Give the extent of all uninfected red blood cells.
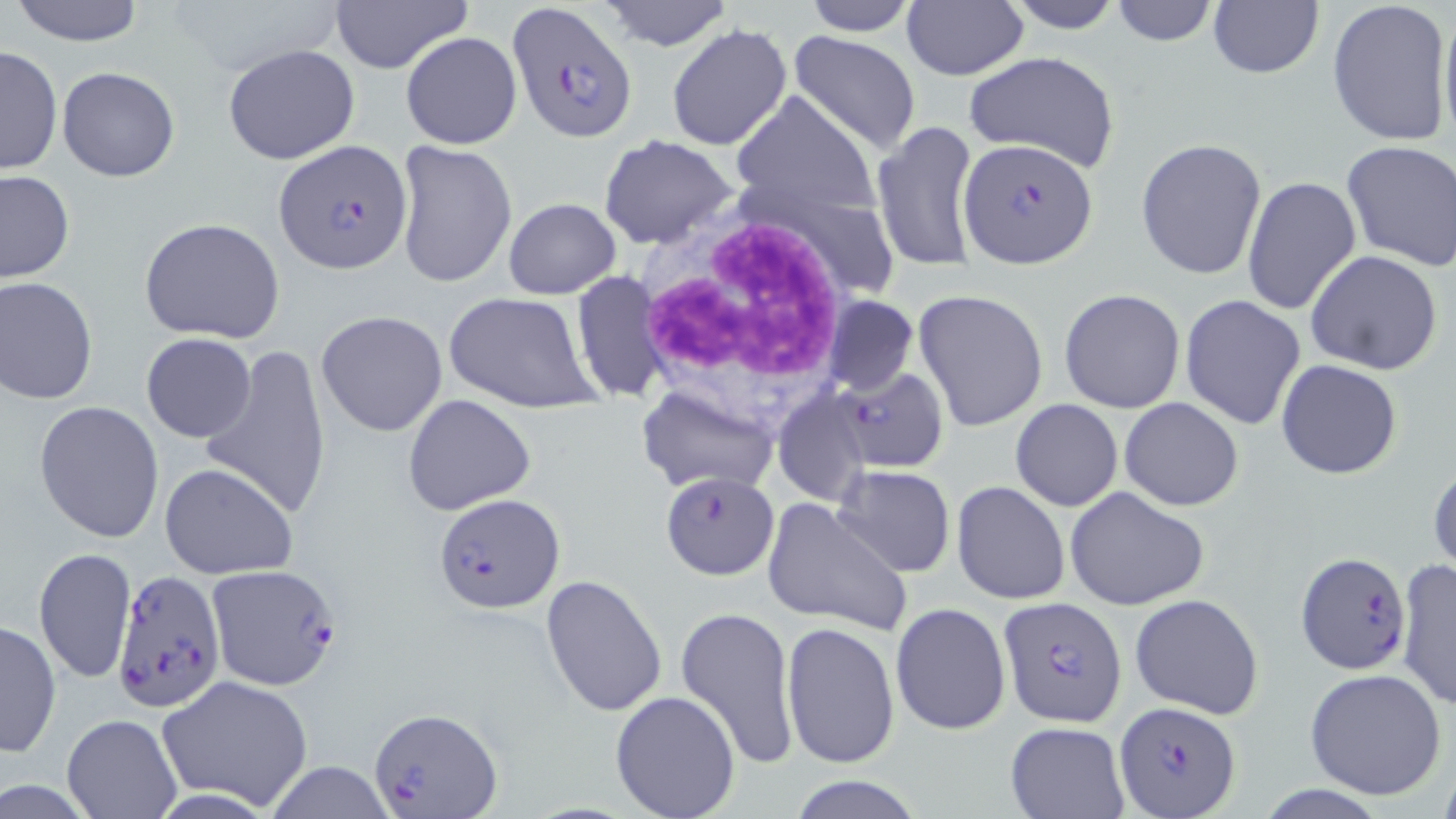

Approximate bounding boxes as named x1/y1/x2/y2 corners in pixels.
Uninfected red blood cells: (x1=7, y1=0, x2=147, y2=47), (x1=326, y1=0, x2=474, y2=73), (x1=598, y1=0, x2=735, y2=50), (x1=800, y1=0, x2=921, y2=36), (x1=1002, y1=0, x2=1128, y2=34), (x1=1109, y1=0, x2=1219, y2=47), (x1=1327, y1=0, x2=1453, y2=147), (x1=1207, y1=1, x2=1325, y2=80), (x1=1438, y1=1, x2=1456, y2=151), (x1=902, y1=2, x2=1029, y2=81), (x1=666, y1=24, x2=791, y2=152), (x1=789, y1=30, x2=922, y2=154), (x1=400, y1=32, x2=522, y2=150), (x1=1, y1=44, x2=61, y2=178), (x1=223, y1=44, x2=362, y2=166), (x1=964, y1=52, x2=1122, y2=173), (x1=56, y1=65, x2=180, y2=181), (x1=731, y1=89, x2=883, y2=222), (x1=872, y1=119, x2=981, y2=274), (x1=597, y1=134, x2=739, y2=249), (x1=1136, y1=138, x2=1268, y2=280), (x1=1341, y1=138, x2=1456, y2=271), (x1=392, y1=140, x2=517, y2=292), (x1=0, y1=170, x2=73, y2=285), (x1=1241, y1=175, x2=1363, y2=316), (x1=504, y1=198, x2=622, y2=300), (x1=138, y1=217, x2=286, y2=344), (x1=1305, y1=249, x2=1444, y2=375), (x1=572, y1=271, x2=666, y2=403), (x1=0, y1=276, x2=99, y2=404), (x1=1058, y1=288, x2=1187, y2=413), (x1=915, y1=290, x2=1048, y2=433), (x1=444, y1=291, x2=601, y2=414), (x1=1180, y1=294, x2=1307, y2=432), (x1=822, y1=296, x2=919, y2=395), (x1=316, y1=311, x2=448, y2=436), (x1=141, y1=332, x2=257, y2=442), (x1=200, y1=346, x2=334, y2=518), (x1=1277, y1=359, x2=1404, y2=480), (x1=638, y1=385, x2=778, y2=497), (x1=773, y1=388, x2=873, y2=506), (x1=402, y1=393, x2=537, y2=516), (x1=1120, y1=397, x2=1244, y2=511), (x1=1010, y1=398, x2=1123, y2=511), (x1=35, y1=400, x2=165, y2=542), (x1=1429, y1=457, x2=1456, y2=578), (x1=158, y1=462, x2=297, y2=579), (x1=832, y1=465, x2=955, y2=577), (x1=952, y1=481, x2=1070, y2=604), (x1=1064, y1=486, x2=1210, y2=611), (x1=762, y1=496, x2=913, y2=636), (x1=32, y1=547, x2=135, y2=687), (x1=1396, y1=561, x2=1456, y2=709), (x1=539, y1=574, x2=669, y2=718), (x1=1130, y1=592, x2=1265, y2=719), (x1=890, y1=602, x2=1011, y2=736), (x1=676, y1=605, x2=799, y2=770), (x1=1, y1=619, x2=62, y2=757), (x1=783, y1=621, x2=899, y2=769), (x1=1304, y1=668, x2=1446, y2=798), (x1=157, y1=674, x2=314, y2=812), (x1=610, y1=690, x2=742, y2=819), (x1=62, y1=714, x2=180, y2=818), (x1=1005, y1=721, x2=1129, y2=818), (x1=265, y1=762, x2=397, y2=819), (x1=787, y1=774, x2=928, y2=818).

White blood cell locations: (x1=633, y1=206, x2=856, y2=441). Plasmodium falciparum-infected red blood cell locations: (x1=507, y1=1, x2=638, y2=142), (x1=960, y1=138, x2=1097, y2=268), (x1=275, y1=141, x2=414, y2=274), (x1=834, y1=367, x2=950, y2=473), (x1=660, y1=471, x2=779, y2=579), (x1=432, y1=491, x2=562, y2=610), (x1=1296, y1=552, x2=1414, y2=675), (x1=205, y1=564, x2=341, y2=689), (x1=110, y1=571, x2=224, y2=713), (x1=1000, y1=598, x2=1127, y2=725), (x1=1113, y1=701, x2=1242, y2=816), (x1=367, y1=707, x2=504, y2=817). Slide-level diagnosis: Plasmodium falciparum. May-Grünwald-Giemsa-stained preparation. Captured at 1000x magnification. Image is 1456×819 pixels. One field of a larger specimen. Optical microscopy. Thin blood smear.